Report the malaria status of this cell.
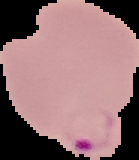
Parasitized.

From a thin blood smear. Segmented cell region on a black background. Image is 139×160 pixels.